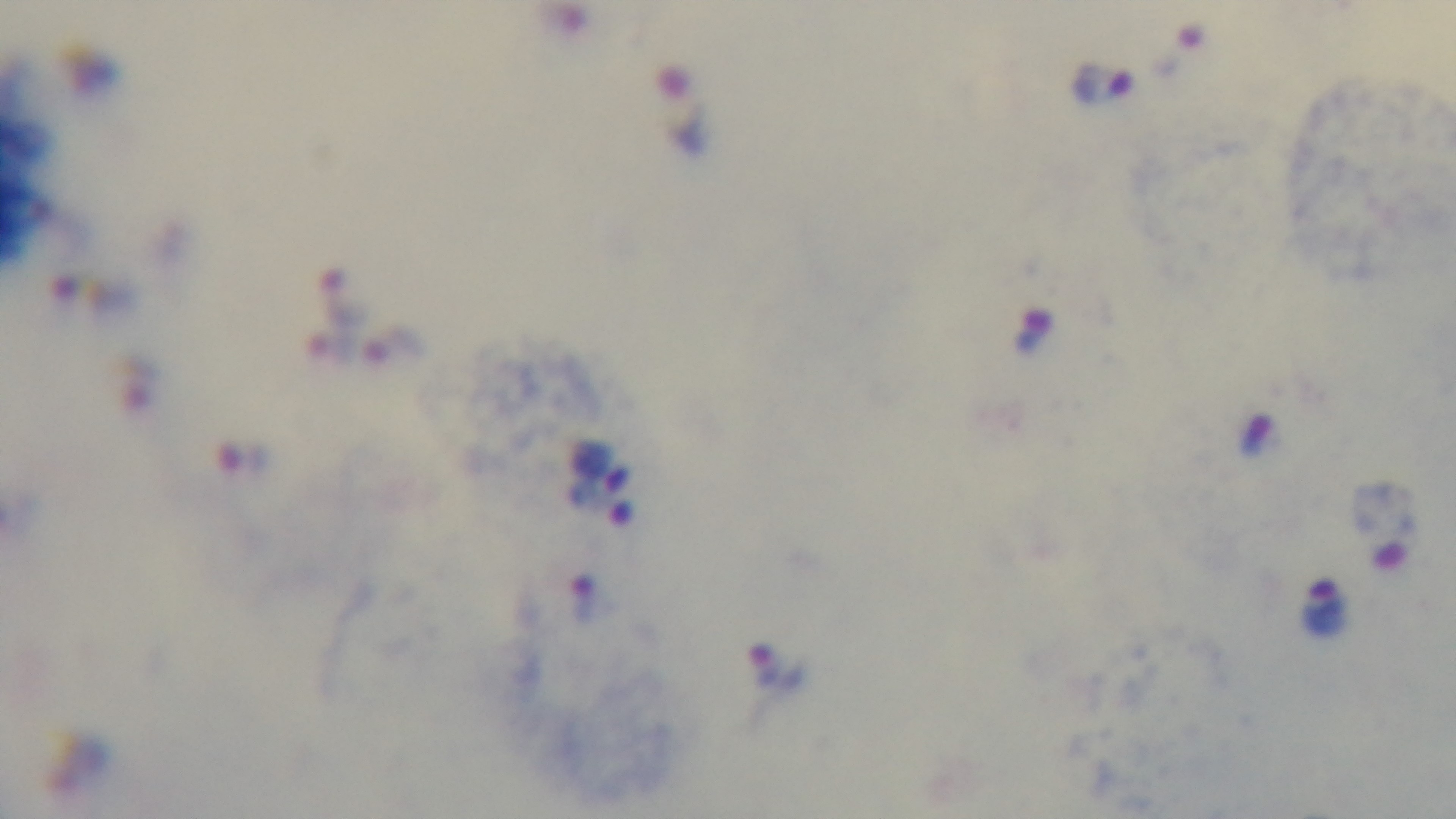 One field from the slide. Giemsa stain. Malaria status: infected. Photomicrograph. 100x oil-immersion objective. Preparation: thick blood film. Mounted 4K digital camera.